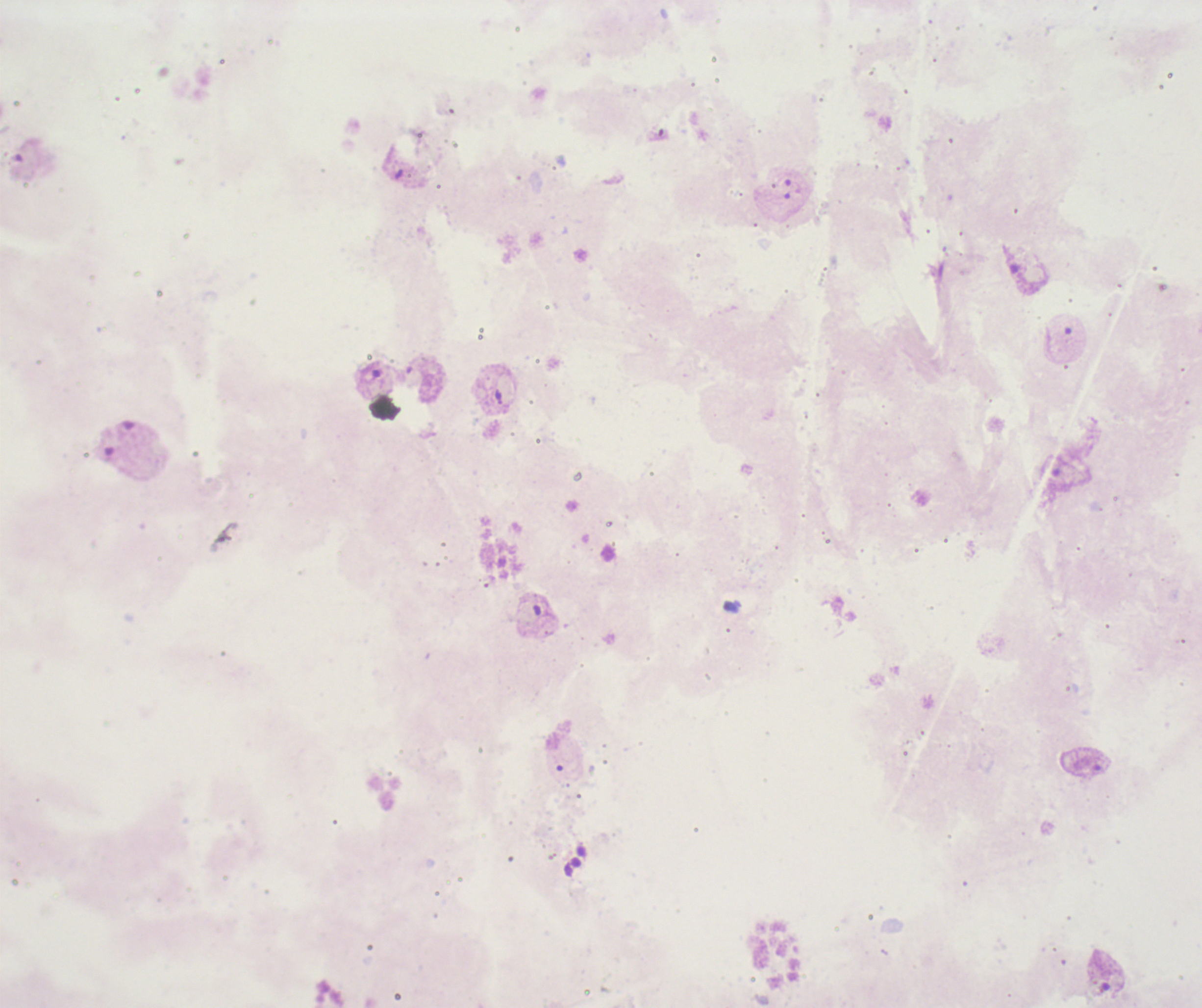

Approximate centers as (x, y) in pixels.
Summary:
  - Trophozoite locations: (1020, 270), (371, 372), (1097, 972)
  - Preparation: thick smear of blood
  - Image size: 1202×1008 pixels
  - Context: previously used in a real diagnosis
  - Coloration quality: bad
  - Background quality: poor
  - Field of view: single
  - Stain: Romanowsky
  - Magnification: 100x
  - Leukocytes: none visible
  - Result: Plasmodium parasites detected